State the blood parasite species.
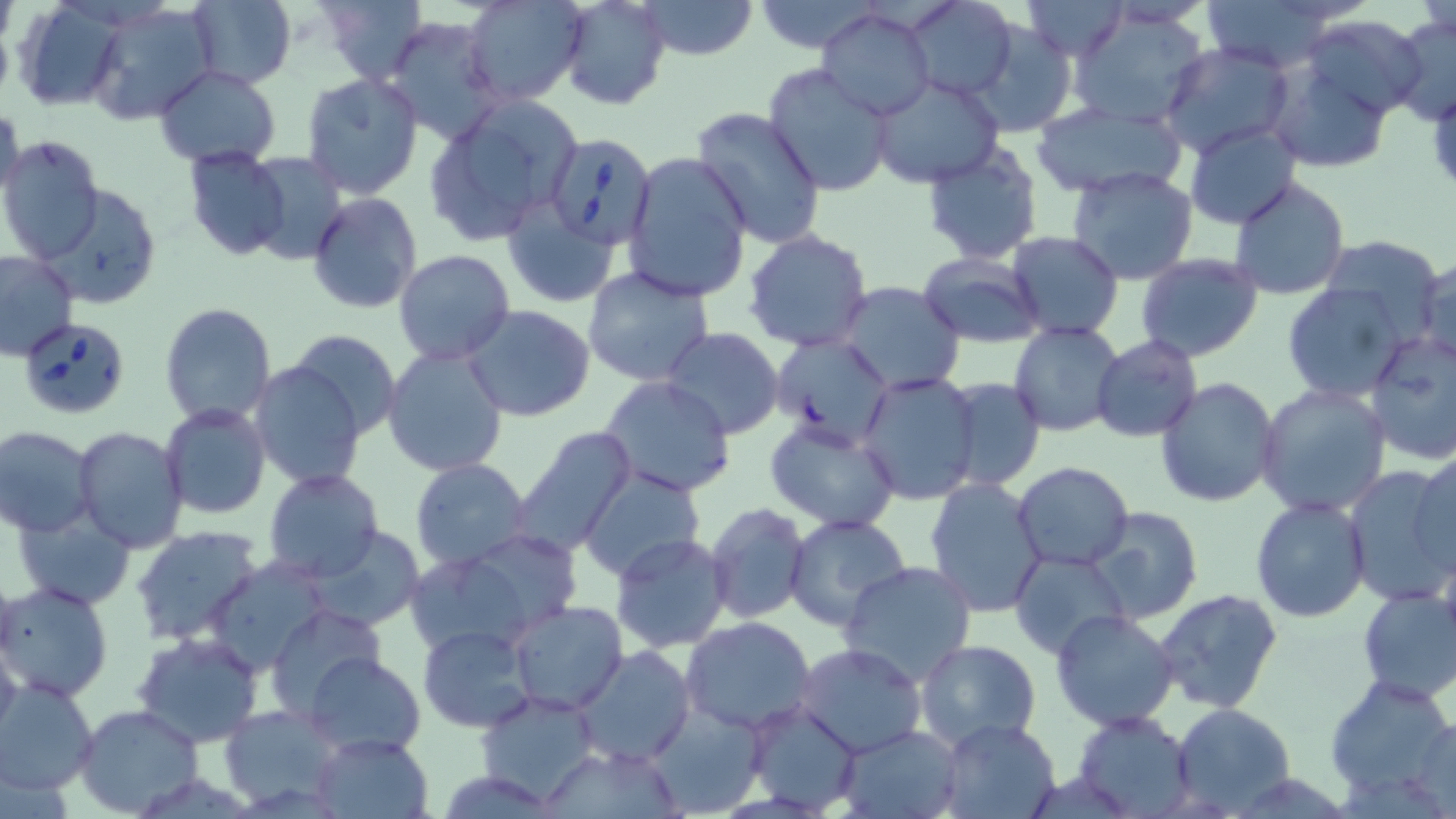
Babesia divergens.

Summary:
  - Coordinate format: approximate bounding boxes as (x1, y1, x2, y2) in pixels
  - Babesia divergens-infected red blood cell locations: (542, 131, 655, 251), (18, 317, 133, 419)
  - Uninfected red blood cell locations: (321, 0, 426, 84), (465, 0, 588, 106), (638, 0, 758, 60), (747, 0, 889, 52), (901, 0, 1020, 101), (1025, 0, 1128, 60), (1197, 0, 1348, 72), (12, 1, 127, 112), (184, 1, 296, 89), (555, 1, 671, 109), (88, 3, 219, 123), (1069, 7, 1213, 130), (817, 8, 934, 121), (1390, 12, 1456, 123), (384, 16, 506, 145), (1303, 16, 1428, 120), (969, 19, 1077, 140), (1159, 42, 1296, 160), (153, 63, 282, 167), (1265, 63, 1396, 173), (762, 64, 893, 197), (300, 73, 424, 200), (870, 75, 1002, 187), (1031, 101, 1187, 197), (0, 102, 25, 211), (466, 102, 580, 209), (689, 107, 828, 252), (1185, 123, 1302, 230), (428, 128, 536, 245), (0, 136, 104, 261), (920, 143, 1045, 265), (182, 148, 293, 262), (247, 151, 347, 267), (621, 151, 754, 303), (1067, 165, 1199, 283), (1227, 176, 1350, 301), (42, 185, 161, 311), (308, 192, 421, 315), (504, 197, 620, 308), (744, 231, 872, 350), (1005, 232, 1125, 341), (1318, 234, 1448, 336), (0, 250, 77, 360), (393, 250, 516, 366), (918, 252, 1046, 347), (1134, 254, 1264, 362), (1415, 256, 1456, 365), (582, 267, 714, 387), (836, 281, 966, 396), (1280, 283, 1410, 402), (159, 302, 276, 427), (464, 304, 596, 422), (1009, 322, 1124, 437), (286, 328, 401, 443), (1365, 328, 1456, 465), (660, 329, 784, 440), (768, 335, 896, 451), (1092, 336, 1203, 442), (383, 344, 511, 479), (249, 360, 367, 490), (856, 371, 982, 504), (599, 375, 736, 497), (940, 376, 1047, 494), (1155, 376, 1282, 506), (1256, 383, 1392, 517), (160, 404, 270, 519), (763, 417, 901, 531), (0, 426, 98, 537), (72, 427, 190, 552), (508, 428, 633, 553), (1410, 450, 1455, 579), (409, 458, 532, 571), (1013, 462, 1134, 570), (1341, 465, 1456, 606), (262, 469, 383, 582), (580, 470, 707, 583), (925, 477, 1050, 618), (1249, 496, 1371, 623), (705, 503, 810, 623), (1085, 506, 1203, 624), (15, 513, 135, 609), (784, 515, 912, 634), (132, 525, 265, 647), (303, 525, 427, 632), (611, 532, 733, 653), (401, 547, 552, 660), (1009, 549, 1132, 661), (205, 559, 332, 675), (836, 561, 978, 686), (2, 581, 113, 702), (1355, 587, 1456, 705), (1155, 588, 1285, 715), (507, 600, 631, 715), (266, 604, 384, 720), (1049, 608, 1179, 731), (682, 617, 818, 737), (418, 624, 535, 733), (0, 630, 23, 745), (133, 633, 263, 748), (914, 639, 1041, 752), (795, 642, 927, 757), (573, 644, 694, 766), (306, 653, 426, 759), (1324, 673, 1456, 803), (0, 678, 99, 796), (476, 689, 601, 805), (744, 699, 863, 814), (645, 703, 767, 817), (75, 704, 205, 817), (1171, 704, 1296, 815), (220, 706, 346, 811), (1072, 710, 1198, 817), (1407, 713, 1455, 812), (940, 717, 1060, 818), (837, 725, 963, 818), (312, 731, 435, 819), (537, 745, 685, 817)
  - Field of view: one of a larger specimen
  - Stain: May-Grünwald-Giemsa
  - Image size: 1456×819 pixels
  - Preparation: thin blood film
  - Modality: light microscopy
  - Magnification: 1000x